Point out each Plasmodium parasite and each leukocyte.
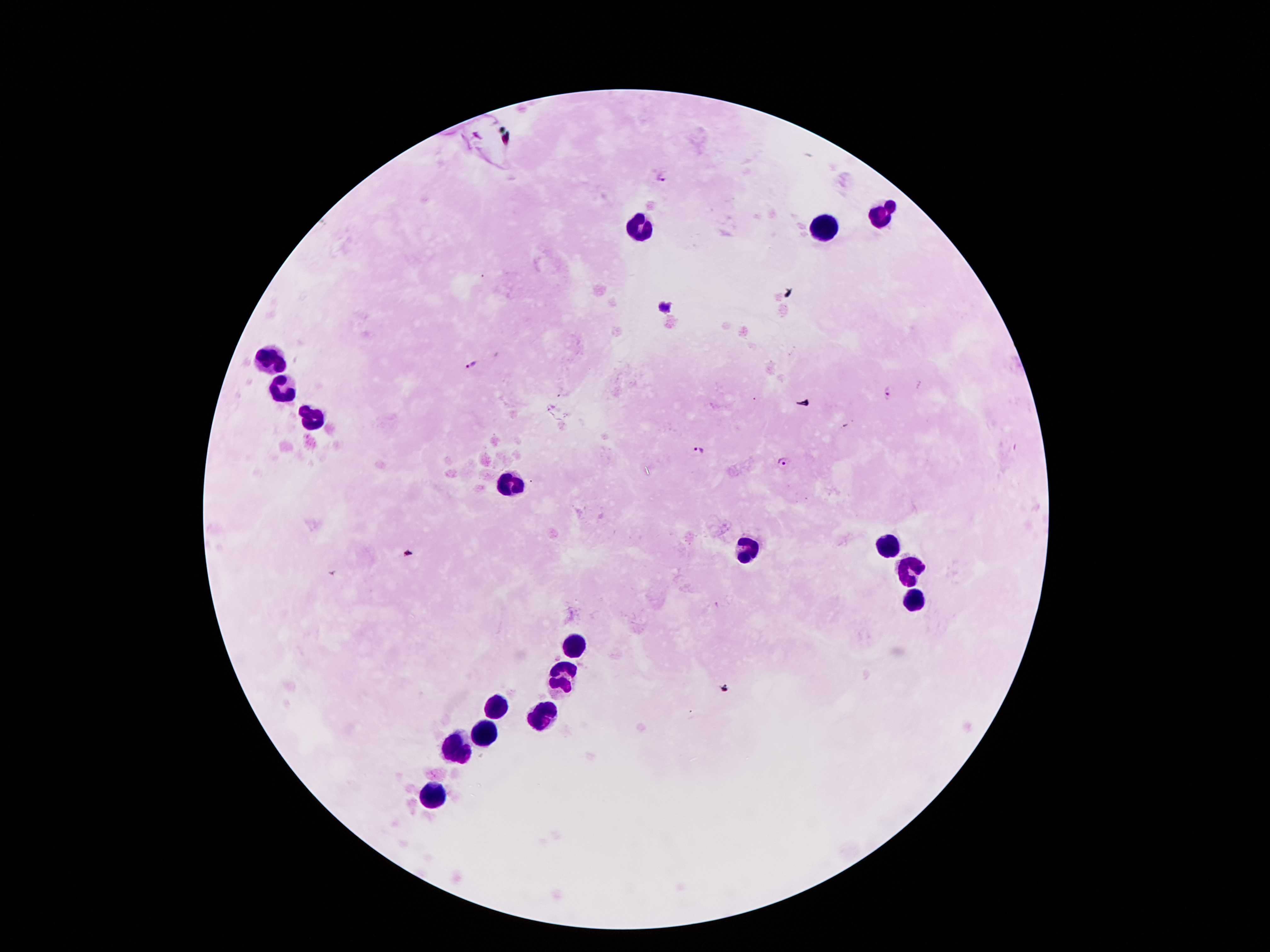

Approximate object centers, in pixels from the top-left corner.
Plasmodium parasites: (x=661, y=176), (x=664, y=309), (x=471, y=365), (x=889, y=396), (x=698, y=451), (x=785, y=463).
Leukocytes: (x=882, y=217), (x=644, y=230), (x=825, y=231), (x=274, y=362), (x=285, y=388), (x=312, y=420), (x=509, y=486), (x=891, y=545), (x=750, y=548), (x=907, y=568), (x=913, y=605), (x=575, y=645), (x=566, y=678), (x=498, y=708), (x=544, y=713), (x=487, y=731), (x=456, y=746), (x=429, y=795).

Image is 1270×952 pixels. Patient malaria status: positive for Plasmodium falciparum. 100x magnification. Single field of view. Thick blood smear. Photographed through the microscope eyepiece with a smartphone camera. Giemsa-stained preparation.